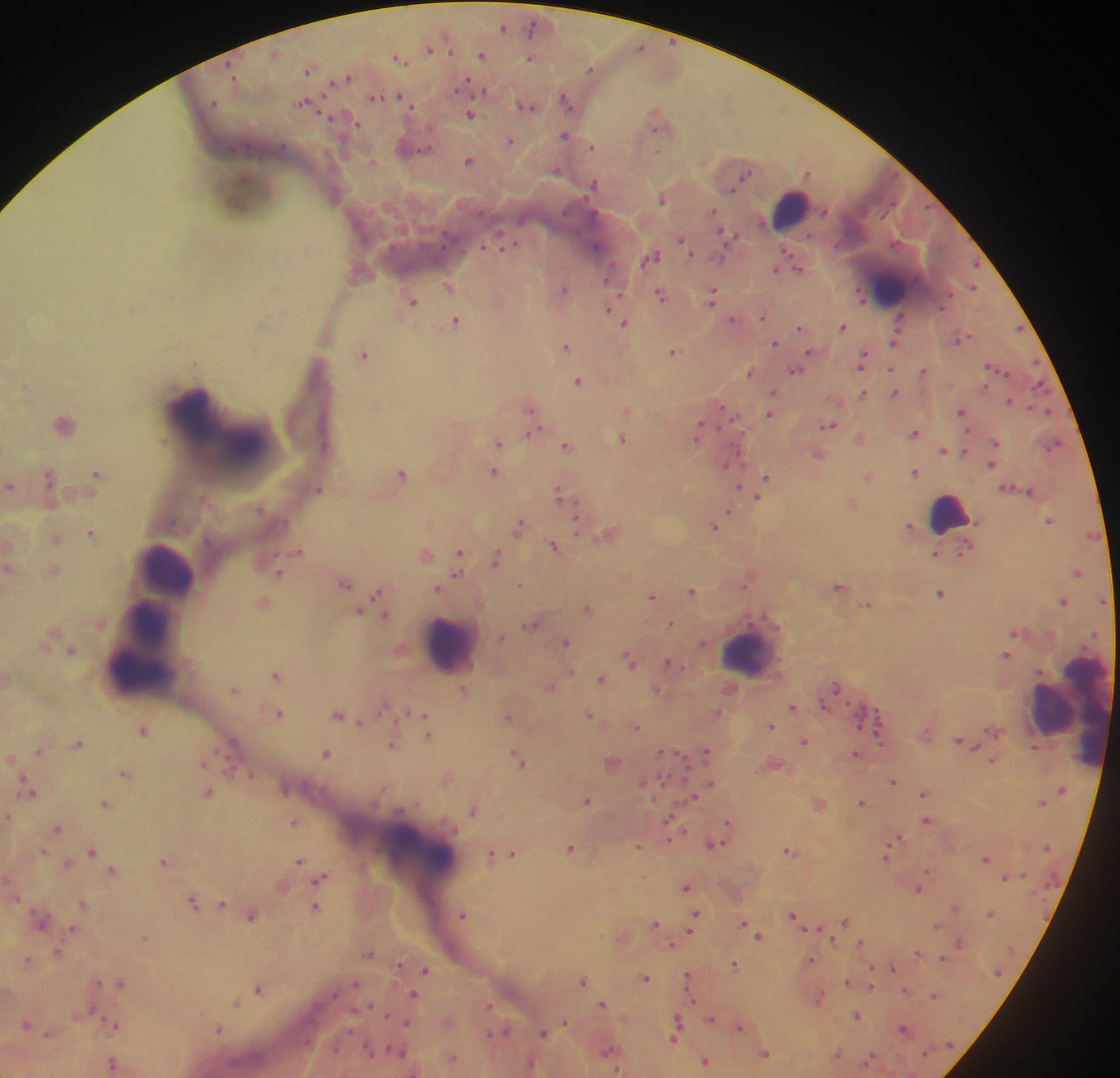 Approximate centers as (x, y) in pixels. Leukocyte locations: (789, 208), (888, 282), (187, 408), (245, 441), (947, 517), (163, 562), (143, 619), (446, 643), (749, 651), (139, 667), (1052, 707), (1092, 711), (419, 846). Malaria parasite locations: (504, 28), (532, 28), (640, 45), (430, 49), (451, 52), (483, 54), (531, 58), (401, 60), (591, 69), (308, 71), (233, 72), (348, 75), (332, 80), (468, 80), (461, 85), (486, 91), (375, 97), (402, 98), (567, 99), (213, 102), (408, 103), (305, 105), (527, 106), (469, 115), (328, 116), (355, 125), (655, 127), (566, 135), (511, 139), (592, 147), (422, 149), (657, 153), (470, 159), (373, 163), (557, 172), (749, 173), (806, 173), (593, 183), (733, 190), (662, 200), (927, 209), (714, 210), (481, 213), (883, 215), (722, 231), (808, 235), (680, 239), (511, 242), (894, 242), (443, 244), (595, 245), (835, 247), (484, 248), (787, 248), (692, 254), (655, 255), (721, 257), (613, 263), (978, 264), (776, 269), (801, 269), (606, 281), (448, 285), (973, 286), (564, 288), (858, 290), (951, 292), (715, 293), (660, 294), (620, 295), (413, 300), (862, 301), (712, 303), (940, 307), (607, 310), (733, 318), (764, 318), (455, 320), (624, 323), (263, 325), (843, 325), (800, 327), (1018, 327), (968, 338), (957, 342), (775, 343), (893, 343), (566, 347), (809, 350), (675, 352), (865, 352), (363, 354), (1035, 360), (992, 366), (891, 368), (924, 369), (998, 370), (796, 371), (750, 373), (1006, 373), (579, 380), (985, 385), (1037, 386), (863, 391), (774, 392), (894, 392), (1010, 401), (723, 405), (530, 407), (1031, 408), (627, 410), (962, 410), (1048, 411), (769, 414), (830, 424), (702, 425), (537, 431), (969, 431), (529, 432), (916, 432), (696, 438), (622, 440), (499, 443), (567, 444), (997, 444), (1055, 447), (944, 450), (964, 451), (725, 464), (743, 464), (992, 464), (494, 472), (915, 473), (403, 474), (95, 476), (766, 476), (50, 478), (868, 478), (740, 487), (319, 489), (561, 491), (1031, 493), (758, 497), (559, 498), (568, 500), (577, 502), (730, 512), (577, 517), (521, 522), (1049, 522), (714, 525), (911, 525), (90, 534), (52, 540), (555, 546), (459, 550), (299, 551), (428, 554), (935, 555), (958, 555), (495, 558), (280, 573), (458, 573), (1077, 574), (345, 583), (520, 585), (838, 588), (438, 589), (692, 589), (378, 593), (940, 594), (653, 598), (1101, 598), (262, 600), (1064, 601), (867, 603), (586, 606), (387, 614), (537, 624), (670, 624), (520, 627), (1015, 633), (1094, 635), (500, 638), (566, 642), (69, 649), (626, 653), (1005, 654), (669, 661), (571, 671), (276, 674), (601, 678), (837, 685), (235, 688), (847, 703), (824, 704), (384, 706), (791, 706), (281, 713), (591, 714), (340, 715), (426, 715), (878, 715), (508, 717), (360, 722), (396, 722), (770, 723), (139, 725), (637, 727), (429, 737), (804, 740), (880, 741), (79, 746), (393, 746), (38, 750), (706, 750), (218, 751), (661, 752), (327, 753), (516, 753), (679, 753), (856, 755), (227, 756), (993, 761), (522, 762), (203, 764), (123, 772), (251, 775), (24, 776), (663, 778), (710, 781), (892, 781), (643, 782), (1060, 789), (209, 792), (285, 792), (923, 794), (695, 797), (587, 799), (862, 801), (1043, 801), (105, 802), (473, 810), (8, 816), (669, 819), (727, 821), (925, 822), (296, 823), (59, 827), (684, 829), (900, 837), (670, 840), (896, 841), (719, 842), (637, 845), (569, 847), (1046, 847), (44, 850), (788, 850), (92, 851), (493, 853), (513, 853), (883, 856), (985, 858), (300, 861), (163, 862), (112, 869), (928, 870), (1024, 873), (323, 876), (1004, 877), (687, 886), (919, 890), (18, 898), (193, 900), (222, 903), (82, 904), (316, 907), (956, 908), (30, 912), (696, 912), (989, 912), (793, 913), (253, 915), (464, 915), (745, 922), (845, 922), (655, 923), (937, 926), (72, 928), (805, 929), (821, 929), (690, 930), (760, 935), (143, 936), (834, 941), (861, 941), (959, 942), (672, 945), (59, 950), (917, 953), (369, 954), (942, 958), (29, 960), (811, 960), (733, 963), (872, 965), (399, 966), (893, 968), (426, 969), (998, 974), (688, 975), (647, 978), (583, 981), (100, 982), (847, 982), (121, 983), (355, 983), (871, 988), (906, 990), (259, 991), (416, 992), (689, 992), (335, 993), (934, 994), (695, 1002), (603, 1003), (236, 1004), (370, 1004), (490, 1005), (354, 1009), (97, 1013), (386, 1015), (676, 1016), (858, 1016), (711, 1018), (565, 1021), (115, 1026), (739, 1026), (903, 1027), (220, 1029), (488, 1031), (506, 1031), (542, 1032), (351, 1033), (48, 1034), (675, 1038), (364, 1044), (950, 1044), (388, 1048), (608, 1050), (925, 1052), (766, 1053), (837, 1054), (871, 1055), (370, 1056), (706, 1062), (530, 1064), (619, 1068). Thick blood film. Collected in Ghana. Single field of view. Photographed through a microscope with a mobile-phone camera. Image is 1120×1078 pixels.